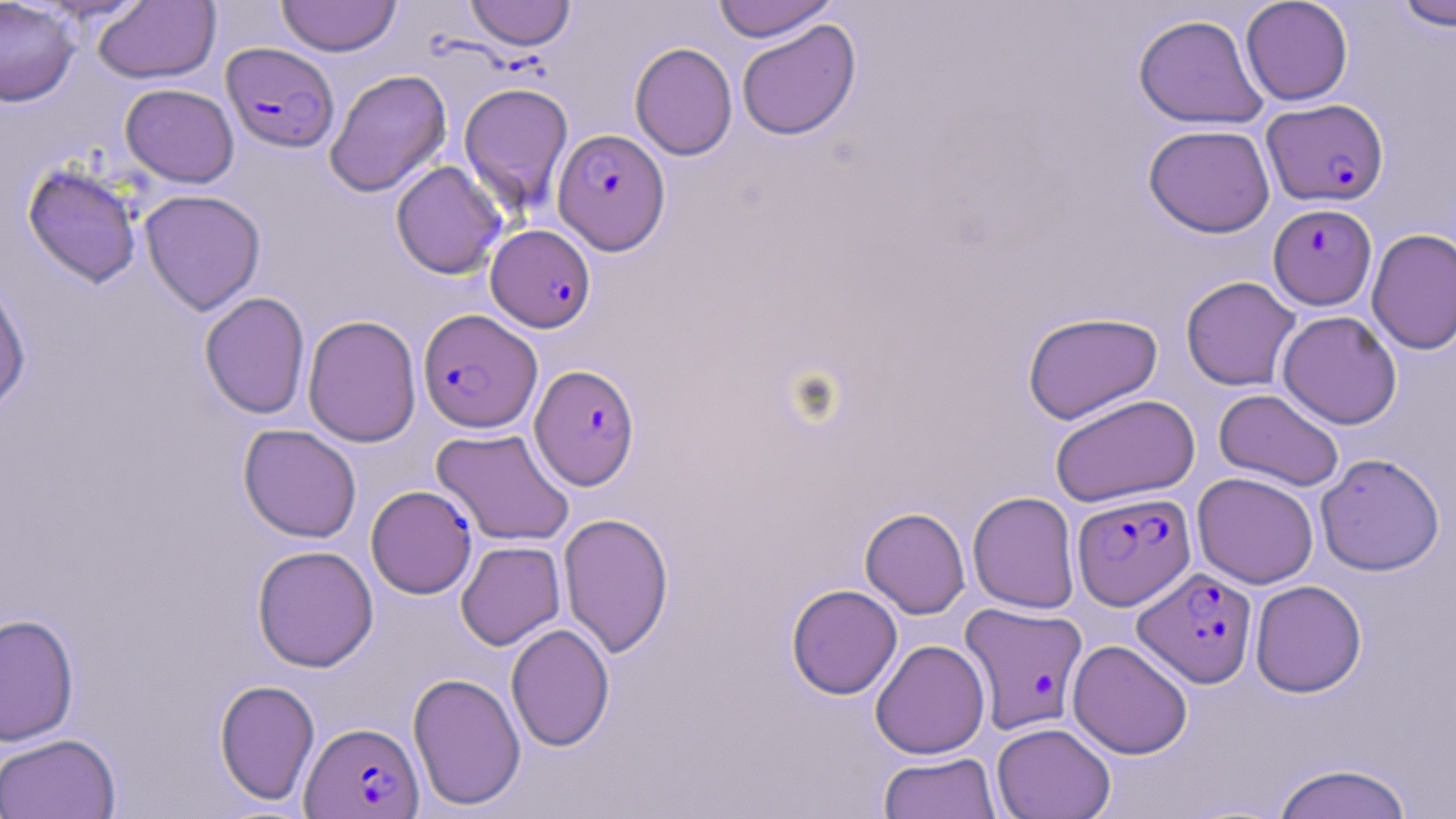

Approximate bounding boxes as (x1,y1)-(x2,y2) corner pairs in pixels. Uninfected red blood cell locations: (0,0)-(81,107), (276,0)-(401,57), (464,0)-(576,50), (711,0)-(840,42), (1240,0)-(1353,105), (1390,0)-(1456,31), (92,1)-(221,84), (1133,13)-(1269,129), (736,19)-(861,140), (629,42)-(738,161), (324,69)-(452,198), (459,81)-(574,218), (120,83)-(239,187), (1143,124)-(1275,237), (22,161)-(143,288), (390,161)-(507,279), (139,189)-(266,315), (1366,228)-(1456,355), (0,274)-(32,417), (1180,275)-(1301,391), (199,292)-(310,419), (1277,310)-(1402,429), (1022,311)-(1163,424), (302,314)-(421,447), (1214,389)-(1345,491), (1050,393)-(1200,507), (238,424)-(362,542), (431,427)-(575,546), (1315,452)-(1445,576), (1192,472)-(1319,589), (967,491)-(1081,613), (859,507)-(970,619), (558,512)-(674,658), (455,540)-(566,650), (252,545)-(379,672), (1250,579)-(1367,698), (787,584)-(902,700), (0,613)-(79,746), (506,623)-(615,752), (870,639)-(990,759), (1067,639)-(1193,759), (407,671)-(526,811), (214,679)-(320,805), (991,722)-(1116,819), (0,733)-(121,819), (878,751)-(1002,819), (1270,762)-(1415,819). Plasmodium falciparum-infected red blood cell locations: (221,42)-(340,153), (1262,98)-(1389,207), (552,129)-(670,254), (1268,203)-(1377,310), (486,224)-(595,332), (418,309)-(542,432), (530,364)-(640,490), (366,485)-(477,598), (1072,491)-(1196,610), (1134,567)-(1258,688), (960,602)-(1088,734), (300,721)-(424,818). Slide-level diagnosis: Plasmodium falciparum. Light microscopy. Thin blood film. Image is 1456×819 pixels. Single field of view. 1000x magnification. May-Grünwald-Giemsa stain.